Locate every blood parasite and identify its species.
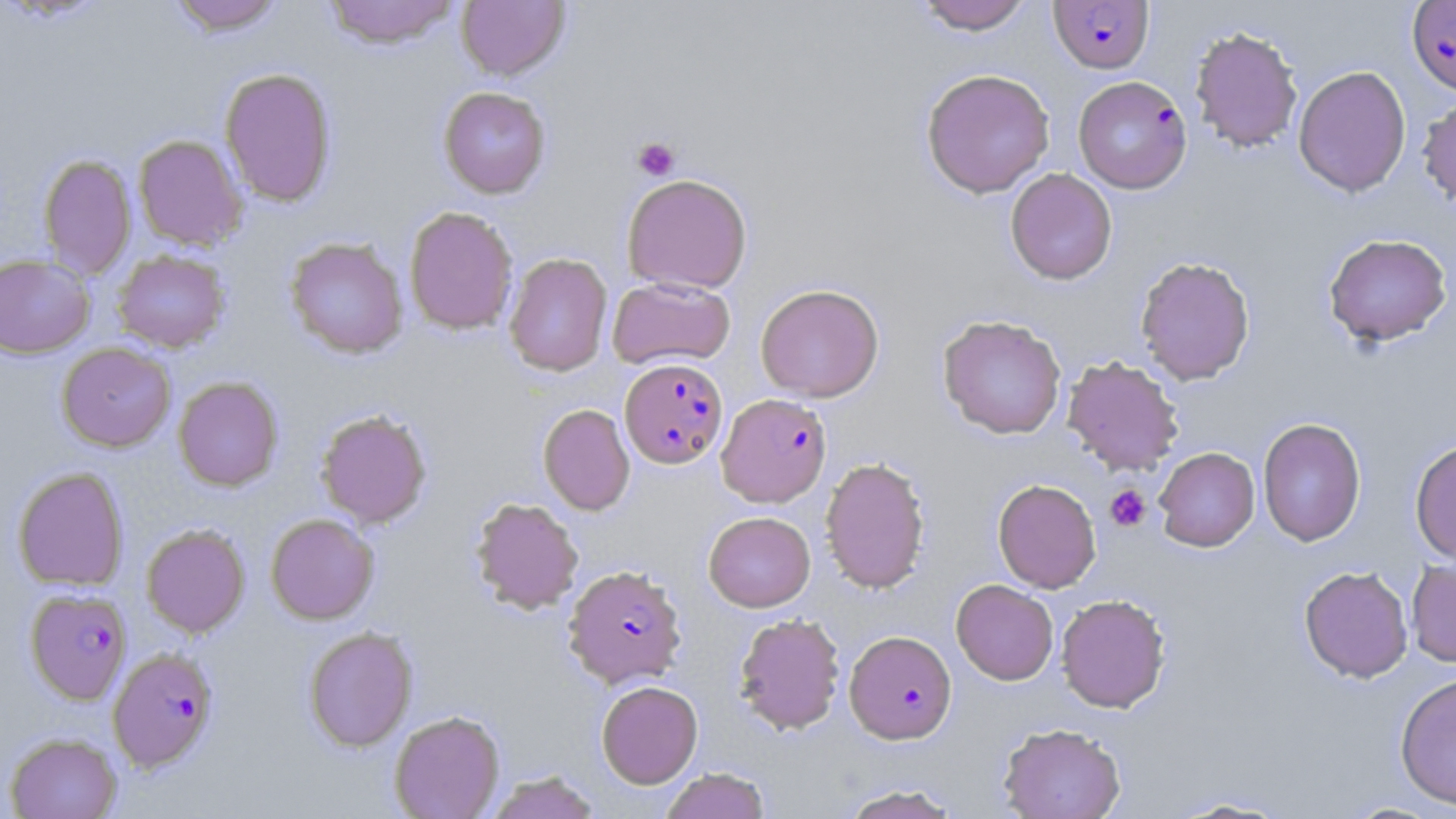
Approximate bounding boxes as (x1,y1)-(x2,y2) corner pairs in pixels.
Plasmodium falciparum-infected red blood cells: (1406,0)-(1456,95), (1049,1)-(1154,74), (1071,77)-(1192,195), (620,358)-(728,469), (717,392)-(832,507), (564,565)-(687,688), (24,588)-(132,705), (844,630)-(957,744), (107,647)-(219,772).
No Plasmodium ovale, Plasmodium malariae, Plasmodium vivax, Babesia divergens, or Trypanosoma brucei observed.

Platelet locations: (632,136)-(680,180), (1104,485)-(1151,532). Uninfected red blood cell locations: (168,0)-(287,36), (321,0)-(461,49), (456,0)-(570,81), (912,0)-(1036,34), (1189,25)-(1303,153), (1293,65)-(1412,197), (219,67)-(337,207), (920,68)-(1055,198), (438,86)-(551,199), (1416,96)-(1456,213), (133,134)-(248,251), (38,153)-(136,280), (1005,168)-(1117,285), (622,173)-(752,294), (404,206)-(519,335), (1323,233)-(1452,346), (285,237)-(409,359), (112,250)-(230,353), (503,252)-(613,376), (0,253)-(95,359), (1135,255)-(1255,385), (607,276)-(736,369), (755,283)-(884,402), (937,314)-(1067,440), (56,342)-(176,452), (1062,355)-(1184,475), (173,376)-(284,491), (538,404)-(635,515), (315,409)-(432,528), (1257,417)-(1366,547), (1409,439)-(1456,565), (1154,447)-(1260,551), (820,456)-(931,593), (12,467)-(129,591), (992,479)-(1102,593), (470,497)-(584,614), (703,511)-(815,612), (266,513)-(379,624), (141,524)-(250,638), (1406,557)-(1456,668), (1299,565)-(1413,683), (951,579)-(1058,685), (1055,593)-(1171,713), (733,613)-(846,736), (303,626)-(417,752), (1394,672)-(1456,811), (596,680)-(703,788), (389,710)-(505,819), (998,723)-(1126,819), (5,732)-(122,819), (660,768)-(770,819), (485,771)-(600,819), (836,783)-(965,818), (1166,795)-(1296,817), (1342,801)-(1446,818). Slide-level diagnosis: Plasmodium falciparum. Captured at 1000x magnification. Thin blood smear. May-Grünwald-Giemsa stain. One field of a larger specimen. Optical microscopy. Image is 1456×819 pixels.